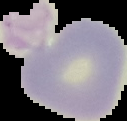
Image is 127×121 pixels. Result: no Plasmodium parasites seen. From a thin blood film. Segmented cell region on a black background.